State the preparation type.
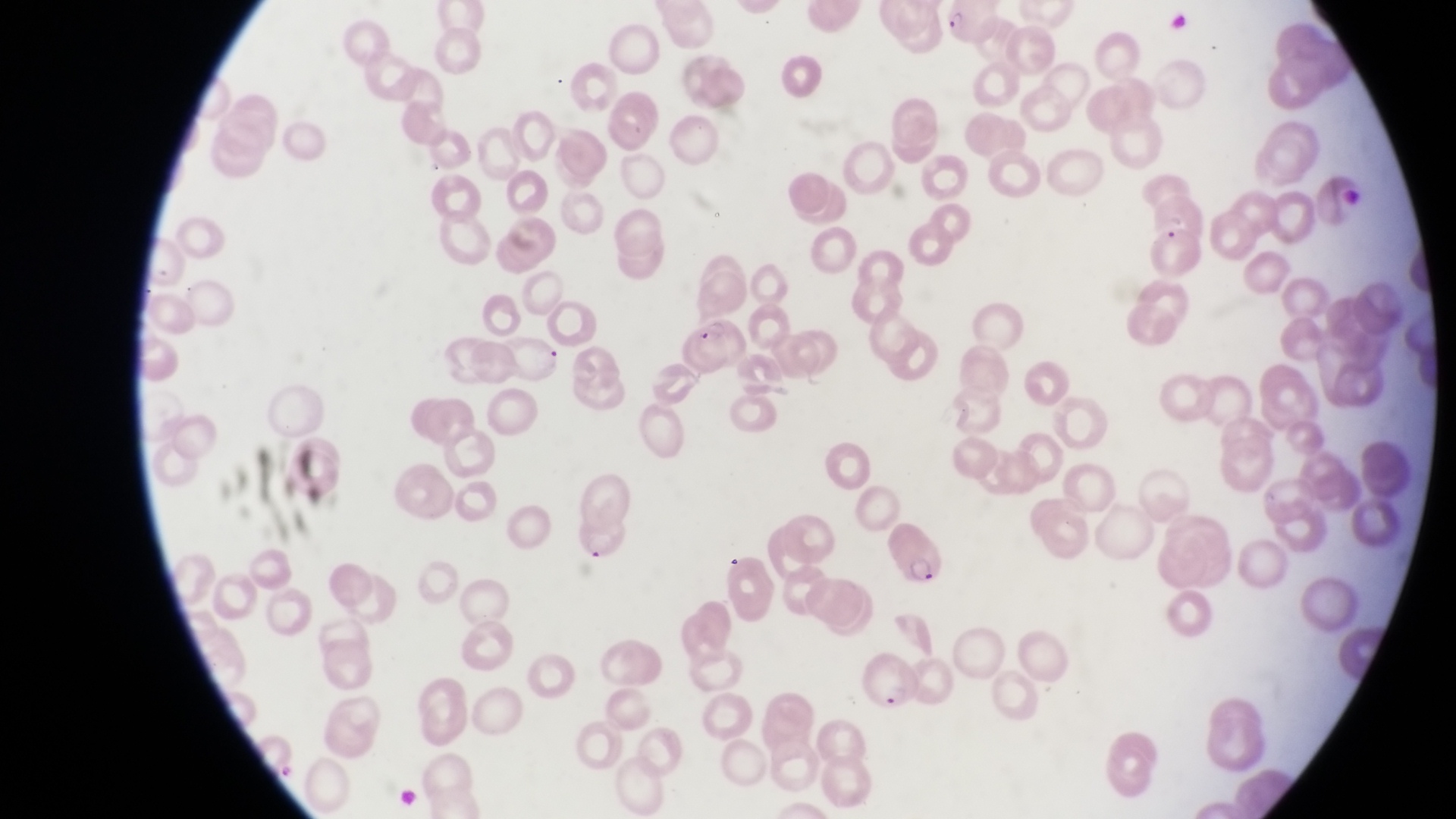
Thin blood film.

Approximate bounding boxes as left top right bottom in pixels. Parasitised red blood cell locations: 948 2 1002 56; 1146 192 1207 248; 679 315 748 375; 574 516 635 572; 883 522 939 583; 854 648 920 711. Captured by a smartphone held over the eyepiece of an Olympus CX-23 microscope. Image is 1456×819 pixels. Magnification of 1000x. Collected in Uganda. Single field of view.